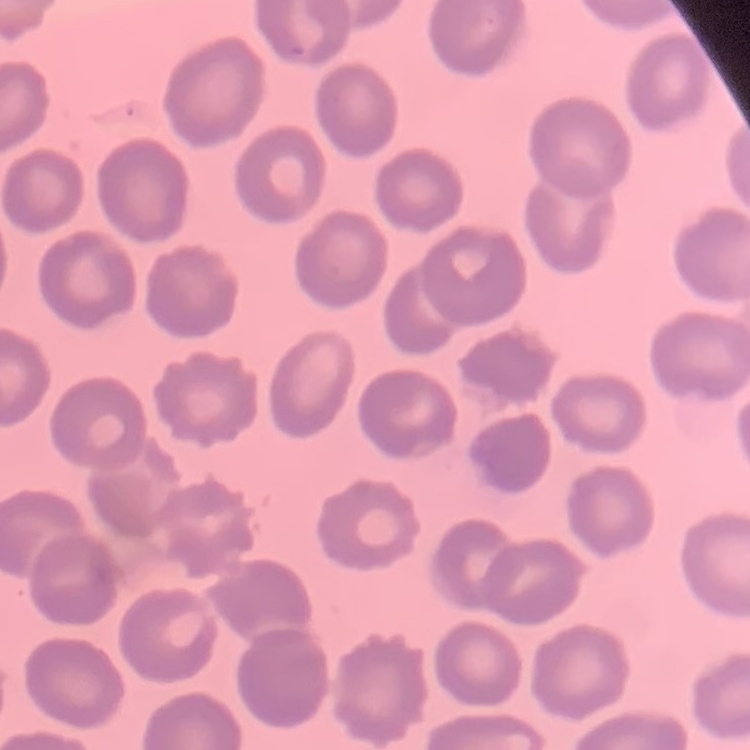
red blood cell morphology = no rouleaux formation
stain = Field's or Giemsa
image type = square crop of a larger photomicrograph
preparation = thin peripheral smear